Point out each Plasmodium parasite.
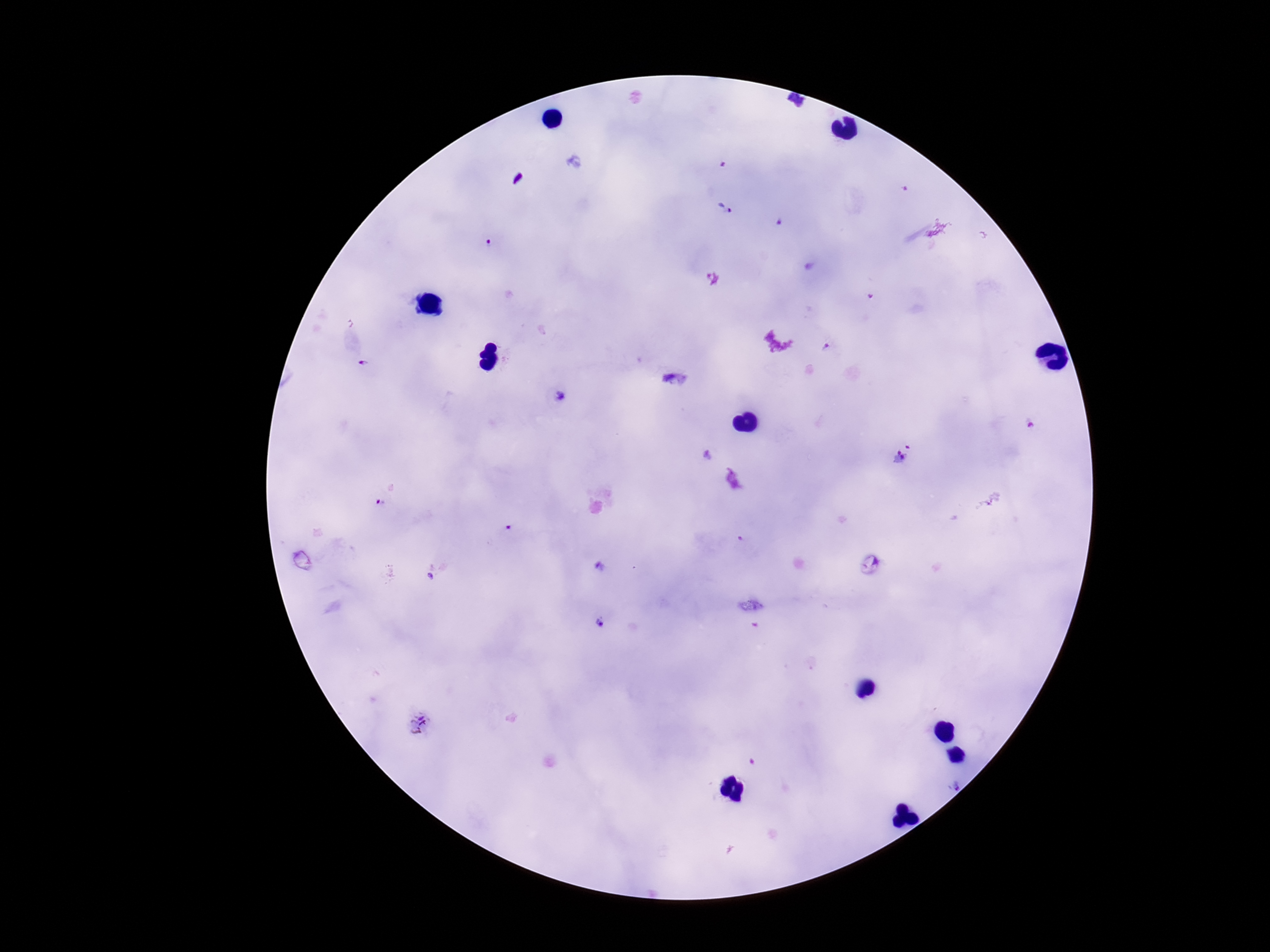

Approximate centers as (x, y) in pixels.
Plasmodium parasites: (902, 190), (726, 207), (491, 243), (827, 345), (368, 366), (559, 397), (1031, 427), (903, 455), (707, 457), (509, 529), (601, 569), (430, 580), (600, 622), (419, 722).

stain = Giemsa
field of view = one from this slide
preparation = thick blood film
capture = smartphone camera through the microscope eyepiece
magnification = 100x
image size = 1270×952 pixels
patient malaria status = positive